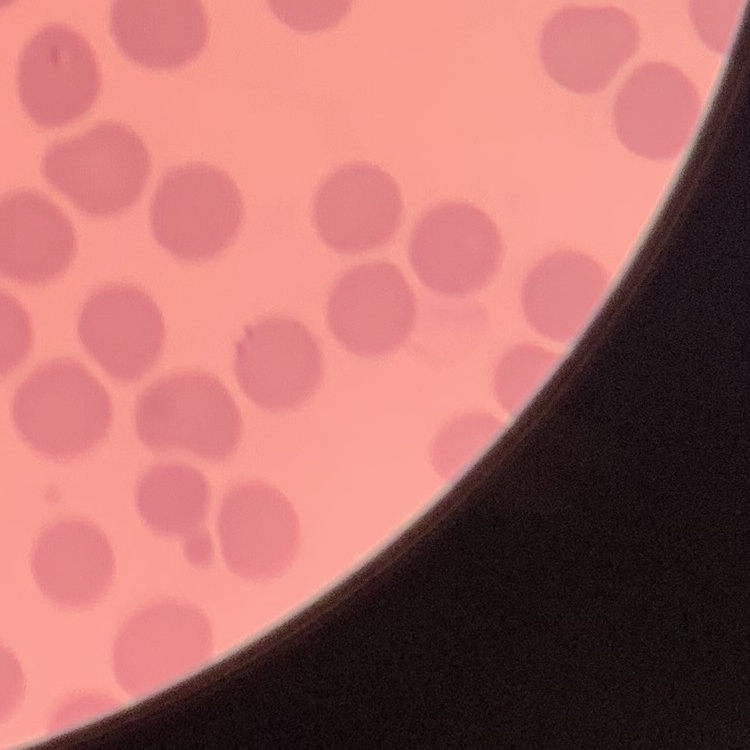

The red blood cells exhibit no rouleaux formation. Square crop of a larger photomicrograph. Thin peripheral smear. Stained with either Field's or Giemsa.